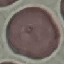

Malaria status: uninfected. Photographed with a smartphone camera at the microscope eyepiece. Giemsa stain. Thin blood film. Automatically extracted cell patch, resized to 64 × 64 pixels.